Report the malaria status of this cell.
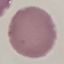

It is uninfected.

image_type: automatically extracted cell patch, resized to 64 × 64 pixels
preparation: thin blood film
capture: smartphone camera at the microscope eyepiece
stain: Giemsa